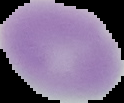
Result: negative for Plasmodium parasites. Segmented cell region on a black background. Image is 124×103 pixels. From a thin blood smear.